Describe the morphology of the red blood cells.
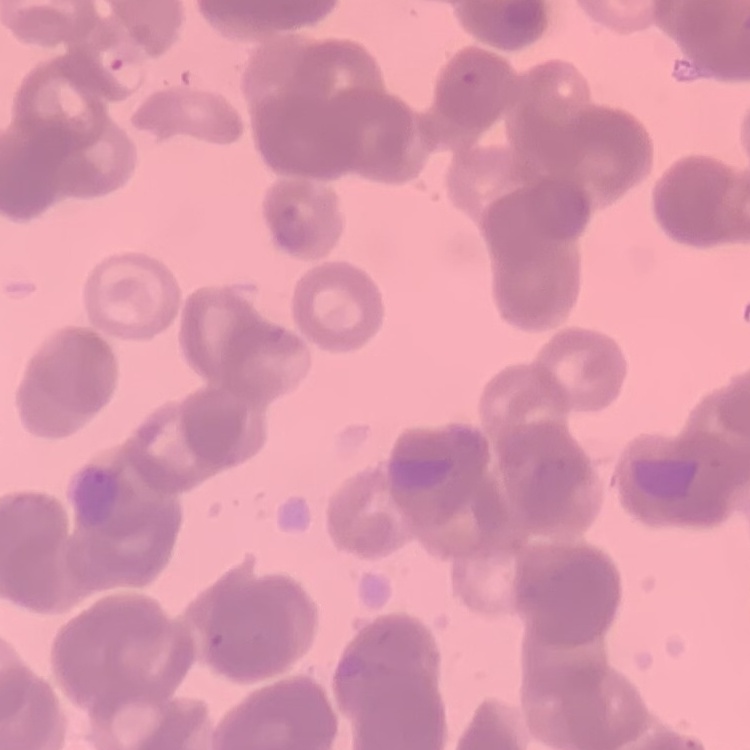

They show rouleaux formation.

Square crop of a larger photomicrograph. Thin peripheral smear. Field's or Giemsa stain.